Locate and identify every blood parasite.
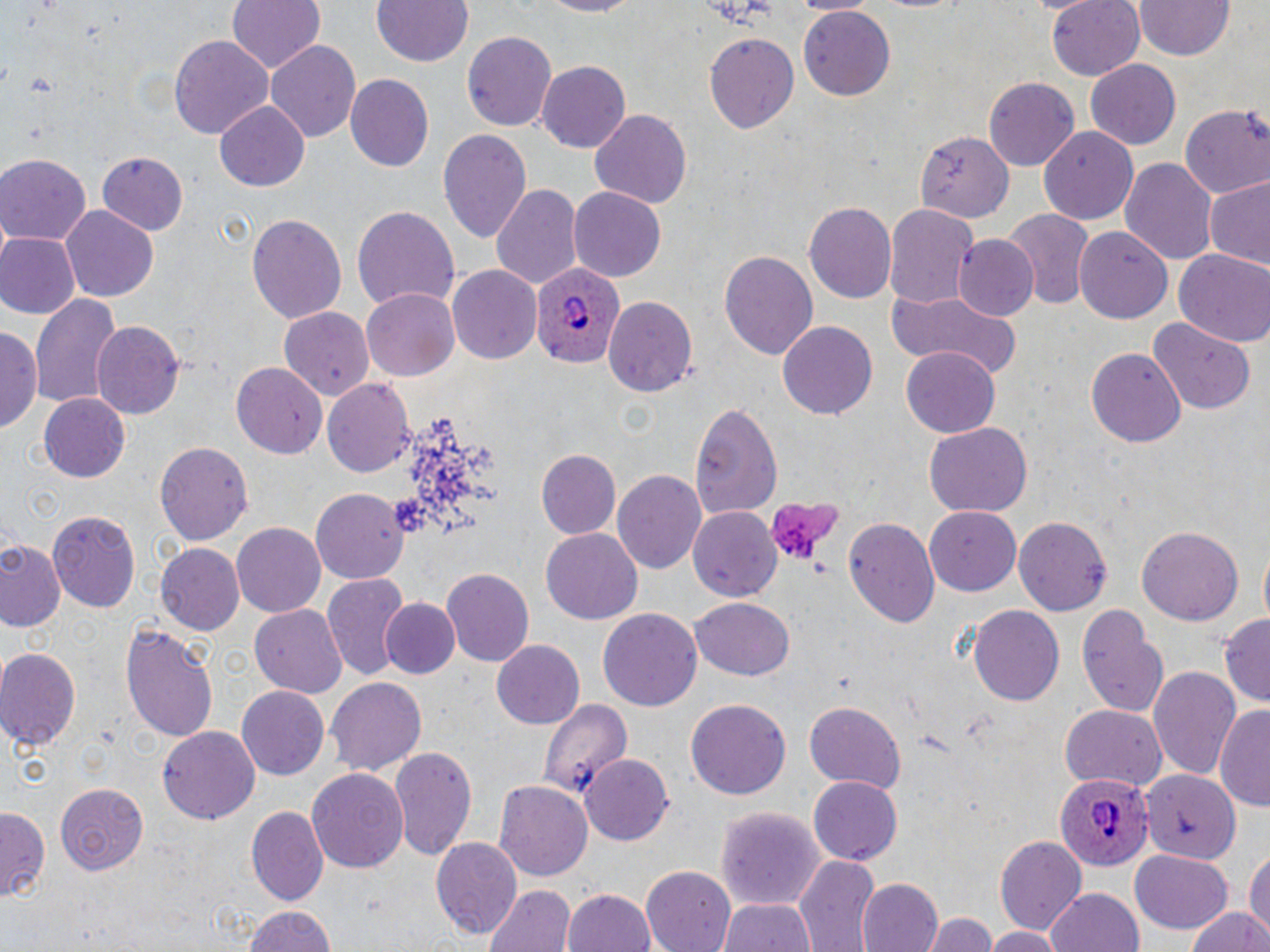
Approximate bounding boxes as named x1/y1/x2/y2 corners in pixels.
Plasmodium ovale-infected red blood cells: (x1=528, y1=261, x2=627, y2=371), (x1=1054, y1=772, x2=1153, y2=874).
No Plasmodium falciparum, Plasmodium malariae, Plasmodium vivax, Babesia divergens, or Trypanosoma brucei observed.

Summary:
  - Platelet locations: (x1=763, y1=493, x2=844, y2=569)
  - Uninfected red blood cell locations: (x1=227, y1=0, x2=325, y2=73), (x1=372, y1=0, x2=473, y2=67), (x1=537, y1=0, x2=647, y2=18), (x1=790, y1=0, x2=877, y2=16), (x1=1045, y1=0, x2=1146, y2=79), (x1=1135, y1=1, x2=1233, y2=61), (x1=800, y1=6, x2=897, y2=101), (x1=461, y1=31, x2=557, y2=132), (x1=705, y1=32, x2=798, y2=133), (x1=167, y1=33, x2=274, y2=140), (x1=265, y1=40, x2=360, y2=145), (x1=1087, y1=61, x2=1181, y2=148), (x1=537, y1=62, x2=629, y2=152), (x1=344, y1=74, x2=433, y2=173), (x1=983, y1=77, x2=1081, y2=171), (x1=216, y1=101, x2=309, y2=190), (x1=1179, y1=104, x2=1270, y2=198), (x1=589, y1=108, x2=692, y2=209), (x1=1038, y1=126, x2=1138, y2=224), (x1=439, y1=130, x2=532, y2=247), (x1=916, y1=134, x2=1013, y2=223), (x1=96, y1=153, x2=188, y2=235), (x1=0, y1=155, x2=90, y2=245), (x1=1119, y1=157, x2=1218, y2=266), (x1=1202, y1=178, x2=1270, y2=270), (x1=489, y1=183, x2=582, y2=293), (x1=568, y1=188, x2=663, y2=282), (x1=802, y1=199, x2=896, y2=301), (x1=884, y1=203, x2=977, y2=307), (x1=351, y1=204, x2=460, y2=311), (x1=63, y1=206, x2=158, y2=303), (x1=1003, y1=208, x2=1095, y2=311), (x1=247, y1=212, x2=346, y2=326), (x1=1075, y1=225, x2=1172, y2=324), (x1=0, y1=232, x2=79, y2=321), (x1=954, y1=235, x2=1038, y2=321), (x1=1174, y1=247, x2=1270, y2=346), (x1=719, y1=250, x2=818, y2=360), (x1=450, y1=266, x2=542, y2=364), (x1=363, y1=287, x2=461, y2=379), (x1=886, y1=289, x2=1025, y2=380), (x1=30, y1=290, x2=119, y2=409), (x1=605, y1=296, x2=697, y2=397), (x1=282, y1=306, x2=373, y2=399), (x1=1149, y1=318, x2=1255, y2=413), (x1=777, y1=319, x2=879, y2=420), (x1=92, y1=323, x2=183, y2=421), (x1=1, y1=325, x2=42, y2=438), (x1=1086, y1=345, x2=1185, y2=444), (x1=899, y1=349, x2=1000, y2=436), (x1=231, y1=361, x2=326, y2=456), (x1=322, y1=380, x2=415, y2=476), (x1=39, y1=392, x2=131, y2=481), (x1=688, y1=400, x2=784, y2=514), (x1=921, y1=422, x2=1032, y2=517), (x1=154, y1=441, x2=253, y2=544), (x1=536, y1=450, x2=619, y2=537), (x1=613, y1=469, x2=707, y2=576), (x1=310, y1=489, x2=409, y2=583), (x1=688, y1=505, x2=781, y2=603), (x1=925, y1=507, x2=1023, y2=594), (x1=47, y1=510, x2=141, y2=614), (x1=1014, y1=515, x2=1113, y2=617), (x1=845, y1=517, x2=940, y2=628), (x1=231, y1=521, x2=326, y2=614), (x1=1138, y1=526, x2=1244, y2=625), (x1=542, y1=529, x2=642, y2=624), (x1=0, y1=540, x2=63, y2=630), (x1=154, y1=543, x2=244, y2=633), (x1=440, y1=568, x2=533, y2=666), (x1=323, y1=574, x2=410, y2=686), (x1=382, y1=599, x2=458, y2=678), (x1=691, y1=599, x2=794, y2=680), (x1=1076, y1=600, x2=1168, y2=721), (x1=249, y1=604, x2=347, y2=695), (x1=967, y1=606, x2=1065, y2=707), (x1=598, y1=608, x2=703, y2=714), (x1=1219, y1=616, x2=1270, y2=705), (x1=120, y1=622, x2=218, y2=742), (x1=491, y1=640, x2=584, y2=728), (x1=0, y1=647, x2=82, y2=749), (x1=1147, y1=663, x2=1241, y2=778), (x1=326, y1=677, x2=426, y2=775), (x1=235, y1=684, x2=329, y2=781), (x1=685, y1=698, x2=791, y2=800), (x1=537, y1=699, x2=632, y2=801), (x1=803, y1=700, x2=906, y2=792), (x1=1216, y1=703, x2=1270, y2=814), (x1=1059, y1=704, x2=1168, y2=790), (x1=160, y1=728, x2=259, y2=821), (x1=390, y1=746, x2=478, y2=864), (x1=581, y1=755, x2=675, y2=845), (x1=307, y1=767, x2=408, y2=877), (x1=1136, y1=772, x2=1244, y2=861), (x1=806, y1=776, x2=902, y2=866), (x1=495, y1=780, x2=593, y2=882), (x1=56, y1=782, x2=148, y2=874), (x1=715, y1=805, x2=827, y2=911), (x1=0, y1=806, x2=48, y2=904), (x1=247, y1=806, x2=329, y2=906), (x1=995, y1=836, x2=1086, y2=935), (x1=431, y1=837, x2=522, y2=938), (x1=1129, y1=848, x2=1233, y2=934), (x1=1246, y1=850, x2=1270, y2=939), (x1=793, y1=854, x2=880, y2=952), (x1=641, y1=867, x2=736, y2=952), (x1=857, y1=876, x2=943, y2=952), (x1=485, y1=884, x2=575, y2=952), (x1=1045, y1=886, x2=1145, y2=952), (x1=563, y1=888, x2=657, y2=952), (x1=718, y1=896, x2=821, y2=952), (x1=240, y1=903, x2=341, y2=952), (x1=1182, y1=908, x2=1270, y2=952), (x1=923, y1=912, x2=997, y2=952), (x1=984, y1=925, x2=1065, y2=952)
  - Slide-level diagnosis: Plasmodium ovale
  - Preparation: thin blood film
  - Image size: 1270×952 pixels
  - Modality: optical microscopy
  - Stain: May-Grünwald-Giemsa
  - Field of view: single
  - Magnification: 1000x